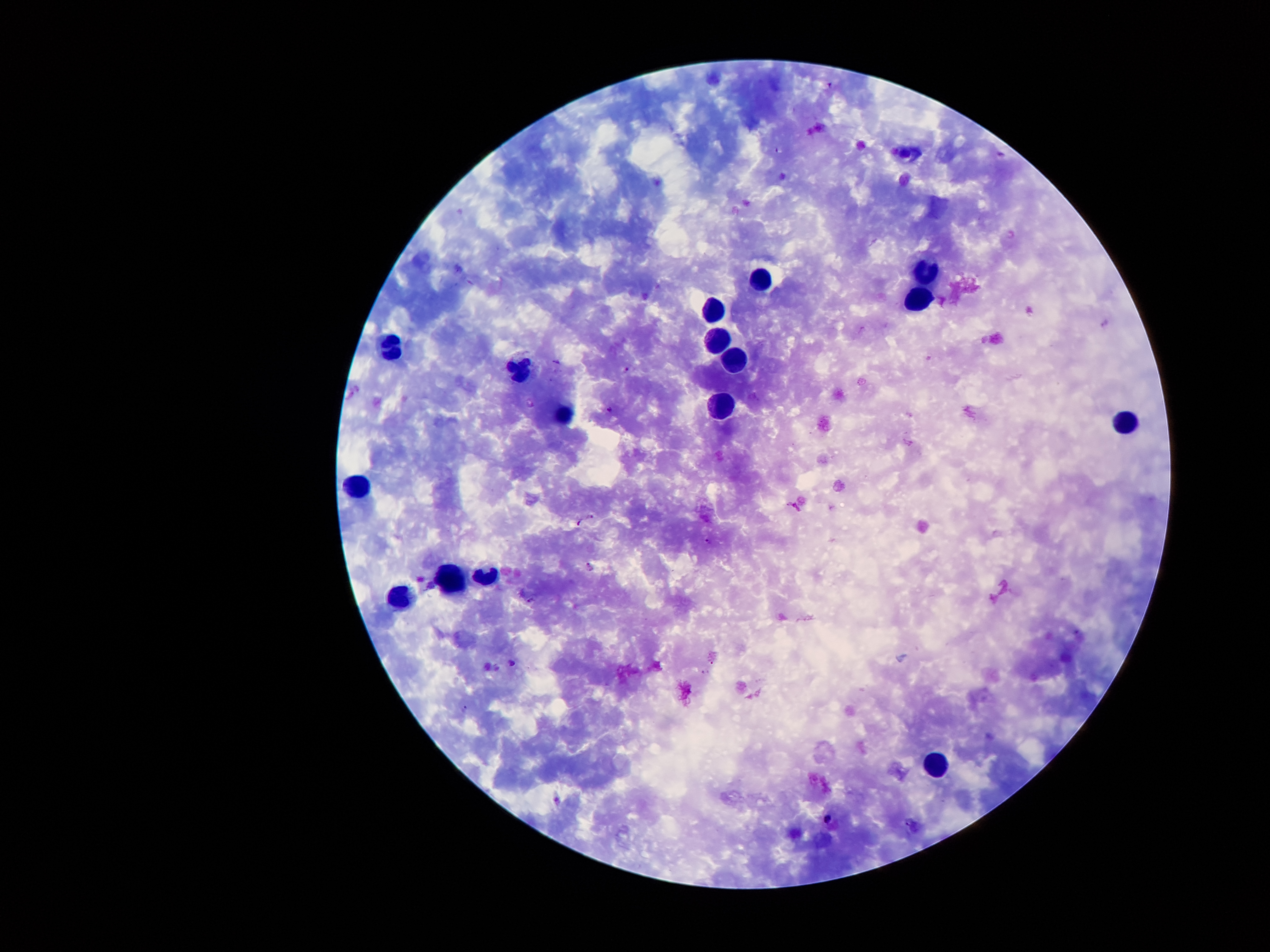
Approximate centers as (x, y) in pixels.
Summary:
  - Plasmodium parasite locations: (831, 85), (776, 149), (557, 362), (627, 369), (608, 409), (592, 517), (580, 524), (707, 540), (588, 566), (530, 600), (512, 663), (465, 708), (827, 818)
  - Leukocyte locations: (928, 272), (761, 282), (916, 294), (710, 312), (713, 341), (392, 349), (734, 359), (514, 367), (717, 409), (566, 415), (1129, 425), (353, 484), (487, 573), (455, 575), (403, 598), (938, 761)
  - Patient malaria status: infected with Plasmodium falciparum
  - Capture: smartphone camera through the microscope eyepiece
  - Preparation: thick blood smear
  - Magnification: 100x
  - Field of view: one from this slide
  - Image size: 1270×952 pixels
  - Stain: Giemsa